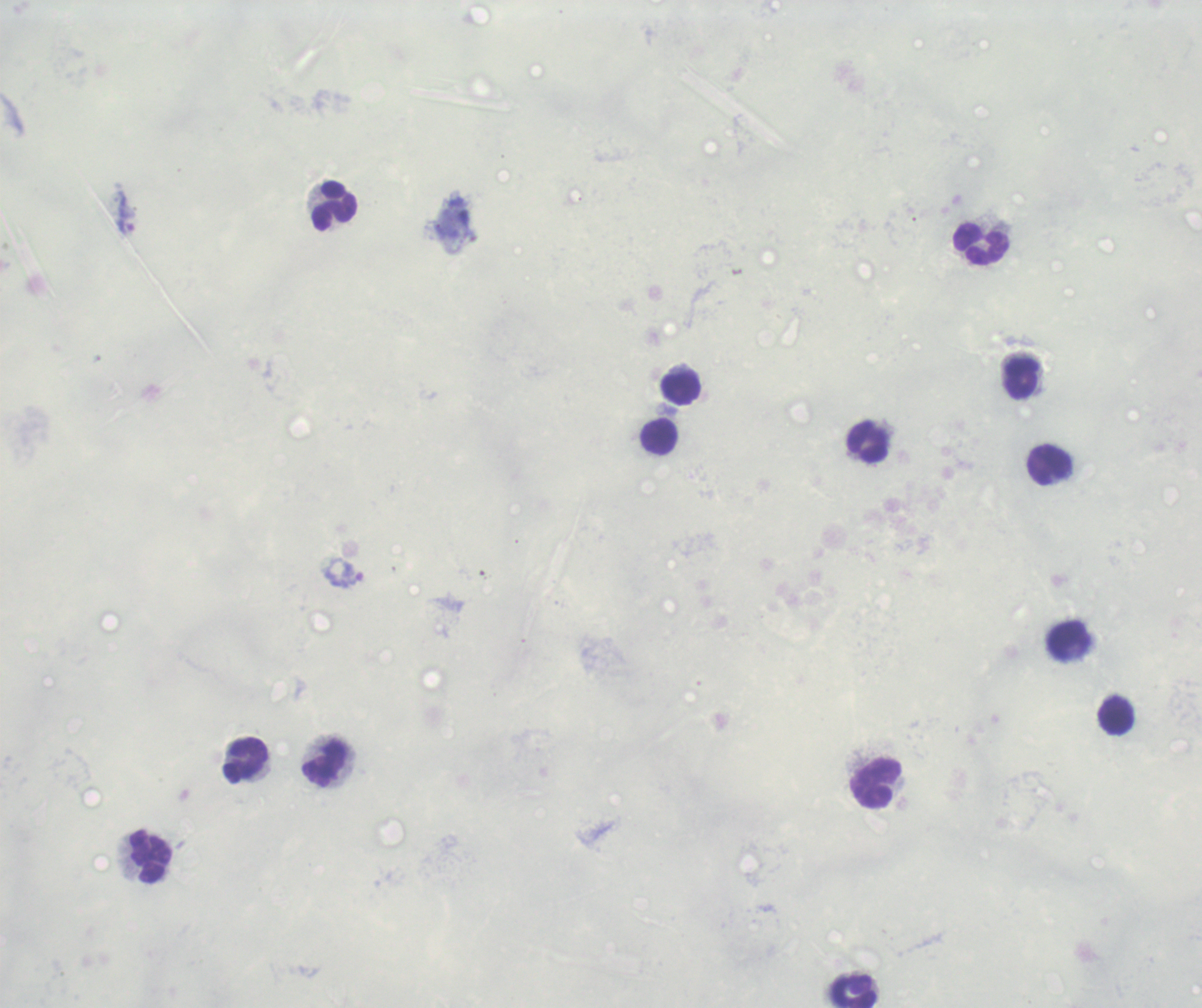
Approximate object centers, in pixels from the top-left corner. Trophozoite locations: (x=127, y=226), (x=345, y=572). Leukocyte locations: (x=335, y=205), (x=982, y=245), (x=1021, y=378), (x=682, y=388), (x=659, y=436), (x=868, y=443), (x=1050, y=465), (x=1068, y=641), (x=1116, y=715), (x=246, y=761), (x=324, y=765), (x=876, y=782), (x=149, y=856), (x=854, y=992). Image is 1202×1008 pixels. Romanowsky-stained preparation. Previously used in a real diagnosis. Thick blood smear. 100x magnification. Result: positive for Plasmodium parasites. Background quality: unsatisfactory. Single field of view.